Locate every Plasmodium vivax-infected red blood cell.
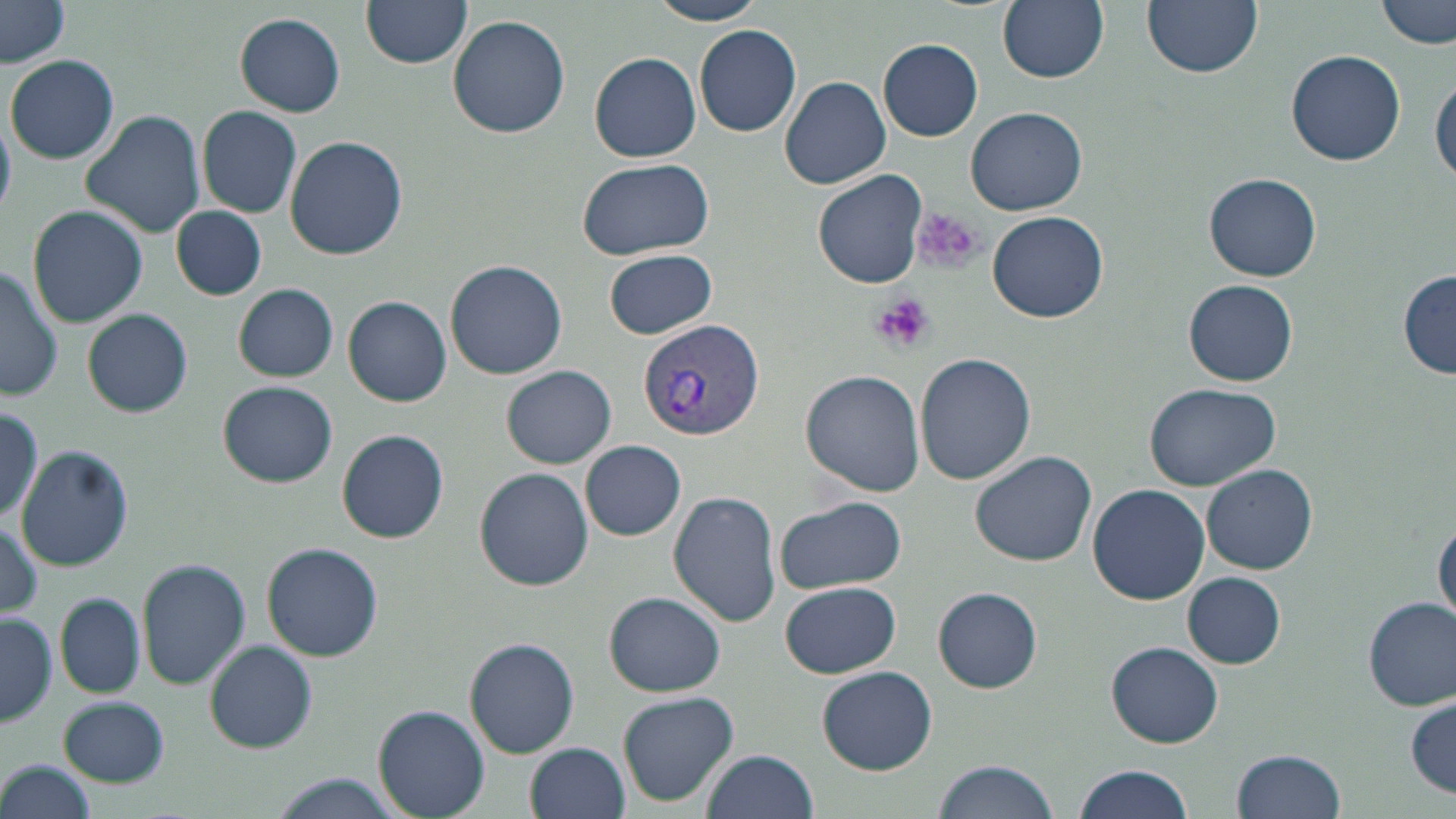

Approximate bounding boxes as (x1, y1, x2, y2) in pixels.
Plasmodium vivax-infected red blood cells: (636, 319, 766, 439).

Platelet locations: (909, 207, 985, 273), (869, 292, 935, 357). Uninfected red blood cell locations: (0, 0, 71, 67), (362, 0, 471, 69), (648, 0, 767, 26), (999, 0, 1109, 83), (1143, 0, 1262, 79), (1377, 0, 1454, 50), (235, 13, 346, 117), (446, 15, 571, 138), (695, 26, 802, 138), (879, 39, 983, 141), (1284, 48, 1407, 168), (589, 51, 702, 163), (6, 55, 118, 165), (780, 74, 892, 189), (1431, 75, 1456, 185), (198, 106, 302, 217), (966, 107, 1088, 216), (81, 109, 206, 238), (284, 134, 410, 259), (575, 158, 713, 260), (812, 168, 928, 289), (1204, 174, 1322, 282), (27, 205, 147, 328), (171, 205, 266, 300), (988, 209, 1108, 322), (604, 248, 717, 340), (445, 259, 568, 379), (0, 263, 63, 397), (1397, 272, 1455, 379), (1183, 279, 1299, 386), (234, 284, 338, 381), (344, 295, 452, 405), (82, 309, 192, 418), (915, 351, 1035, 484), (502, 366, 616, 467), (800, 370, 926, 498), (218, 380, 337, 487), (1146, 382, 1278, 491), (2, 399, 44, 527), (337, 429, 449, 543), (580, 440, 686, 540), (17, 445, 134, 572), (969, 450, 1096, 568), (1201, 465, 1318, 576), (475, 468, 593, 591), (1087, 483, 1211, 606), (669, 491, 782, 628), (773, 495, 908, 593), (1, 517, 43, 617), (1434, 518, 1456, 628), (262, 541, 382, 660), (136, 558, 251, 689), (1183, 572, 1285, 667), (779, 581, 902, 678), (933, 587, 1041, 692), (606, 591, 727, 695), (56, 592, 146, 697), (1363, 598, 1455, 710), (0, 614, 58, 727), (463, 638, 579, 757), (204, 639, 317, 752), (1106, 641, 1223, 748), (816, 665, 937, 775), (617, 691, 741, 807), (1406, 695, 1454, 799), (59, 696, 170, 787), (374, 705, 490, 817), (526, 742, 631, 819), (1232, 748, 1345, 819), (701, 749, 819, 819), (931, 760, 1061, 818), (1, 762, 97, 816), (1070, 764, 1199, 819), (269, 775, 406, 819). Slide-level diagnosis: Plasmodium vivax. Image is 1456×819 pixels. Light microscopy. Single field of view. Captured at 1000x magnification. May-Grünwald-Giemsa stain. Thin blood smear.